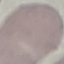

Result: no malaria parasites detected. Acquired by smartphone through the microscope eyepiece. Giemsa-stained preparation. Thin smear of blood. Cell patch, automatically extracted from a larger field of view and resized to 64 × 64 pixels.